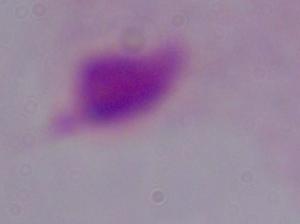
modality: micrograph
identification: trichomonad
magnification: 1000x